Classify this cell by malaria status.
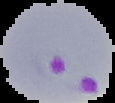
Parasitized.

{
  "image_type": "segmented cell region on a black background",
  "image_size": "115×103 pixels",
  "preparation": "thin blood smear"
}